Outline each Trypanosoma brucei.
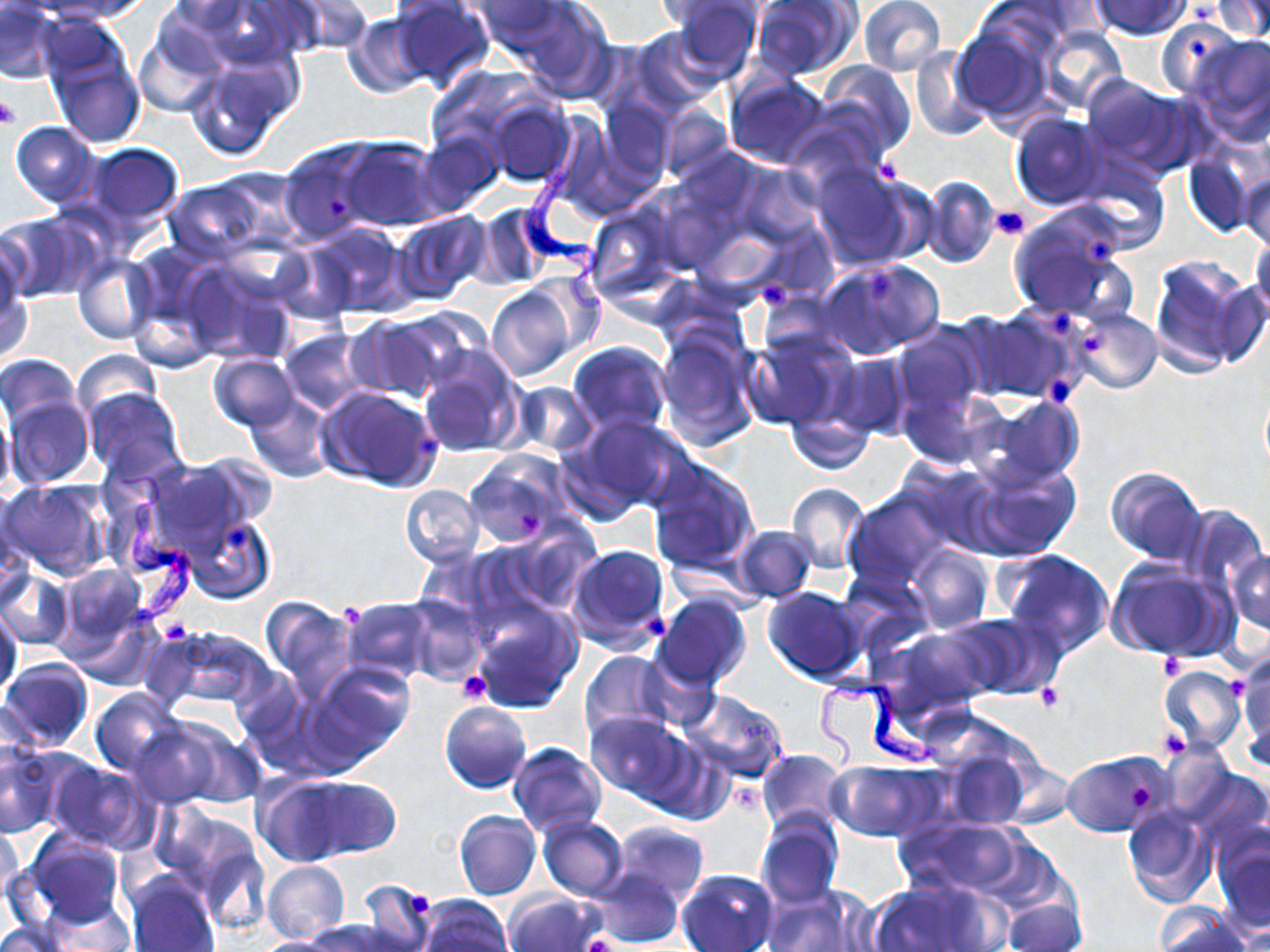
Approximate bounding boxes as (x1, y1, x2, y2) in pixels.
Trypanosoma brucei: (513, 112, 606, 314), (108, 465, 200, 631), (813, 671, 941, 778).

Uninfected red blood cell locations: (50, 0, 153, 21), (160, 0, 261, 46), (464, 0, 578, 56), (652, 0, 759, 29), (666, 0, 762, 82), (751, 0, 858, 81), (858, 0, 945, 76), (1089, 0, 1192, 39), (1207, 0, 1269, 41), (179, 1, 305, 69), (279, 1, 373, 55), (389, 1, 495, 91), (508, 1, 618, 102), (0, 2, 63, 84), (342, 13, 433, 98), (1154, 19, 1244, 101), (41, 22, 148, 148), (952, 23, 1052, 123), (1039, 25, 1127, 112), (627, 27, 725, 117), (135, 30, 224, 118), (1186, 31, 1270, 142), (909, 44, 990, 141), (186, 54, 301, 160), (818, 60, 916, 158), (1079, 73, 1191, 172), (723, 75, 832, 169), (599, 95, 675, 186), (486, 99, 576, 187), (658, 104, 733, 184), (1010, 112, 1109, 210), (9, 121, 99, 207), (416, 130, 504, 215), (337, 137, 445, 231), (278, 139, 385, 245), (86, 143, 183, 225), (1185, 149, 1259, 238), (1077, 156, 1167, 249), (734, 162, 823, 246), (812, 165, 923, 271), (1240, 172, 1270, 254), (919, 175, 1001, 268), (162, 180, 273, 264), (471, 204, 553, 289), (584, 204, 682, 302), (1008, 207, 1133, 323), (2, 211, 100, 303), (392, 212, 489, 304), (303, 222, 414, 319), (1249, 234, 1270, 326), (120, 245, 228, 370), (72, 253, 156, 344), (1148, 254, 1260, 377), (0, 256, 31, 365), (181, 259, 299, 367), (819, 260, 943, 358), (487, 286, 575, 382), (1072, 307, 1162, 393), (966, 308, 1080, 403), (346, 314, 456, 403), (655, 327, 758, 451), (893, 327, 985, 416), (279, 329, 372, 413), (742, 329, 853, 430), (568, 342, 673, 436), (415, 348, 525, 459), (74, 349, 163, 423), (828, 353, 912, 439), (207, 354, 297, 431), (0, 356, 81, 432), (513, 382, 597, 456), (1259, 384, 1270, 476), (315, 386, 443, 491), (897, 387, 992, 471), (80, 388, 187, 487), (245, 394, 334, 483), (5, 395, 93, 488), (979, 396, 1086, 487), (785, 409, 875, 475), (568, 414, 689, 515), (464, 451, 571, 548), (968, 457, 1081, 560), (138, 458, 260, 556), (646, 459, 758, 573), (908, 464, 1004, 556), (1103, 465, 1206, 564), (1, 479, 111, 581), (786, 482, 868, 573), (400, 486, 481, 566), (844, 489, 948, 587), (1178, 501, 1267, 595), (184, 513, 276, 605), (732, 526, 816, 603), (490, 528, 595, 616), (565, 543, 671, 653), (908, 544, 993, 633), (997, 547, 1114, 659), (1227, 549, 1270, 641), (1107, 558, 1230, 661), (55, 563, 148, 654), (1, 569, 74, 651), (761, 587, 867, 683), (654, 594, 751, 691), (258, 596, 358, 697), (403, 597, 487, 684), (341, 598, 437, 685), (470, 600, 581, 711), (66, 604, 163, 691), (0, 606, 23, 701), (954, 613, 1061, 700), (153, 624, 276, 711), (892, 627, 996, 717), (579, 650, 676, 741), (1232, 652, 1270, 759), (631, 653, 720, 731), (0, 660, 93, 752), (308, 663, 414, 764), (1158, 666, 1246, 756), (91, 688, 184, 776), (680, 690, 790, 784), (440, 701, 531, 793), (585, 713, 689, 802), (128, 721, 223, 807), (171, 725, 268, 808), (0, 739, 64, 839), (938, 740, 1034, 830), (507, 742, 609, 838), (755, 749, 848, 834), (1061, 749, 1168, 836), (44, 758, 148, 850), (827, 761, 938, 841), (1182, 765, 1270, 851), (254, 775, 355, 866), (298, 778, 401, 859), (1122, 804, 1215, 909), (454, 810, 540, 901), (757, 811, 843, 910), (538, 817, 629, 901), (901, 817, 1026, 896), (610, 822, 709, 905), (0, 823, 24, 912), (1212, 828, 1270, 938), (22, 831, 123, 928), (197, 845, 270, 936), (262, 861, 349, 943), (676, 868, 777, 952), (590, 869, 684, 947), (125, 871, 220, 952), (357, 879, 439, 952), (869, 881, 996, 952), (763, 884, 874, 952), (505, 891, 602, 952), (418, 895, 513, 952), (1001, 899, 1085, 952), (1154, 904, 1250, 952), (308, 920, 402, 951), (0, 921, 69, 952), (246, 936, 348, 951). Platelet locations: (0, 96, 20, 129), (876, 158, 900, 184), (990, 205, 1031, 242), (1087, 235, 1115, 262), (862, 269, 892, 301), (755, 280, 792, 309), (1053, 311, 1068, 336), (1083, 336, 1105, 352), (1048, 375, 1071, 405), (416, 435, 435, 462), (518, 511, 541, 537), (226, 525, 251, 553), (644, 614, 669, 639), (162, 618, 193, 643), (1160, 653, 1188, 681), (457, 670, 492, 702), (1230, 673, 1245, 695), (1035, 683, 1064, 713), (1157, 728, 1190, 762), (1129, 785, 1156, 814), (409, 887, 432, 915), (585, 933, 618, 952). Slide-level diagnosis: Trypanosoma brucei. Thin blood smear. Light microscopy. Captured at 1000x magnification. Single field of view. Image is 1270×952 pixels. May-Grünwald-Giemsa stain.